Rate the background quality.
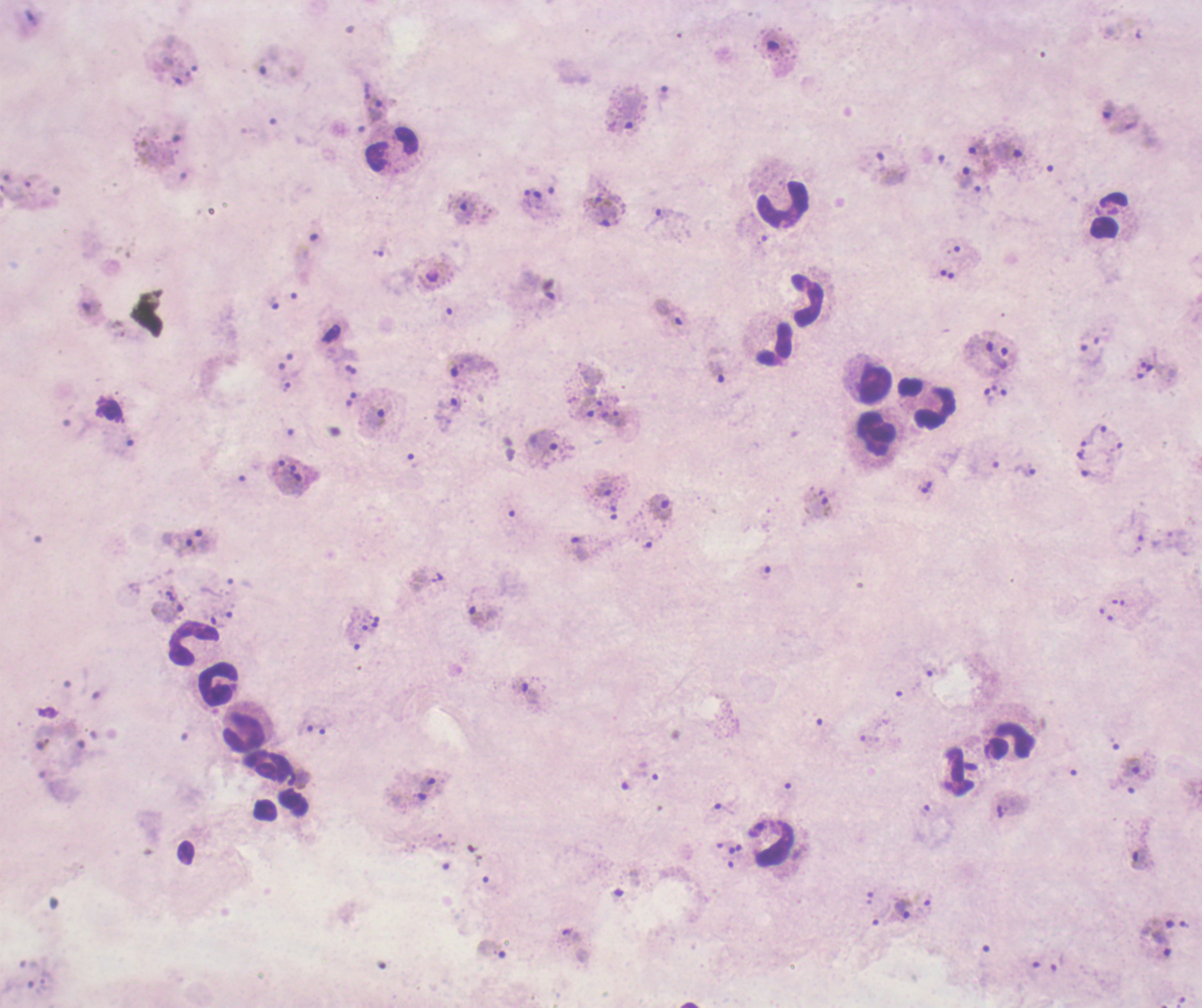

Poor.

{
  "life_cycle_stages_observed": "trophozoite, gametocyte",
  "preparation": "thick blood film",
  "context": "previously used in a real diagnosis",
  "trophozoite_locations": "approximate centers as [x, y] in pixels: [664, 93], [376, 109], [627, 112], [1010, 152], [889, 167], [966, 177], [462, 211], [603, 216], [663, 218], [273, 303], [669, 315], [1002, 356], [467, 364], [718, 373], [989, 396], [448, 413], [613, 418], [373, 420], [1090, 433], [543, 443], [1027, 470], [294, 478], [605, 489], [660, 506], [818, 509], [202, 541], [478, 616], [531, 695], [306, 726], [1131, 767], [427, 784], [1139, 859], [902, 908], [1185, 924], [1157, 941], [491, 950]",
  "field_of_view": "single",
  "gametocyte_locations": "approximate centers as [x, y] in pixels: [778, 45]",
  "image_size": "1202×1008 pixels",
  "stain": "Romanowsky",
  "magnification": "100x",
  "leukocyte_locations": "approximate centers as [x, y] in pixels: [392, 148], [784, 204], [1108, 215], [807, 300], [775, 344], [875, 387], [935, 407], [877, 434], [194, 644], [220, 686], [246, 732], [1012, 740]",
  "result": "Plasmodium parasites identified",
  "coloration_quality": "bad"
}